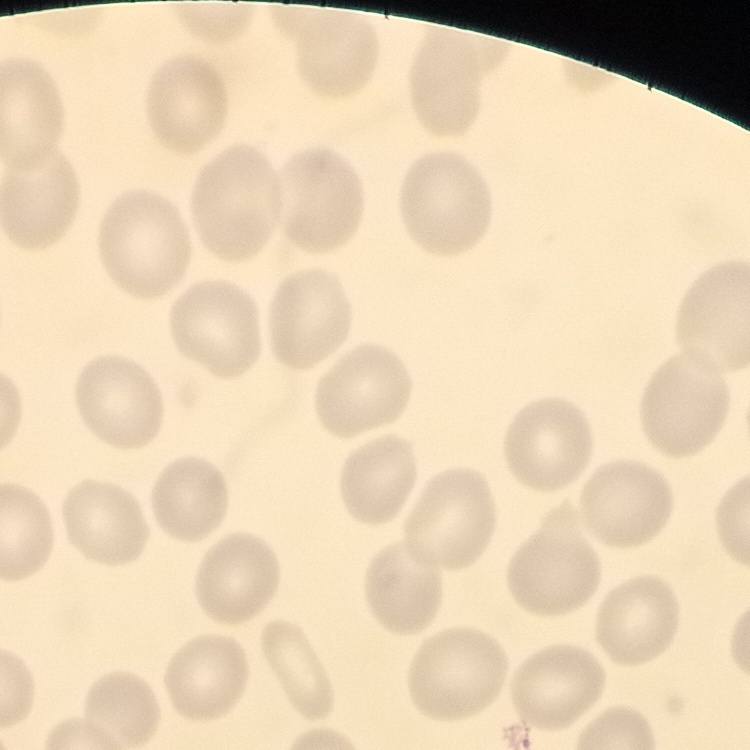

Summary:
  - Red blood cell morphology: no rouleaux formation
  - Image type: one tile cut from a larger photomicrograph
  - Preparation: thin blood film
  - Stain: Field's or Giemsa